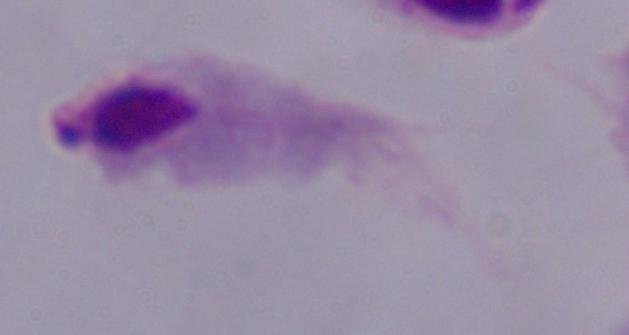

Summary:
  - Identification: trichomonad
  - Magnification: 1000x
  - Modality: photomicrograph